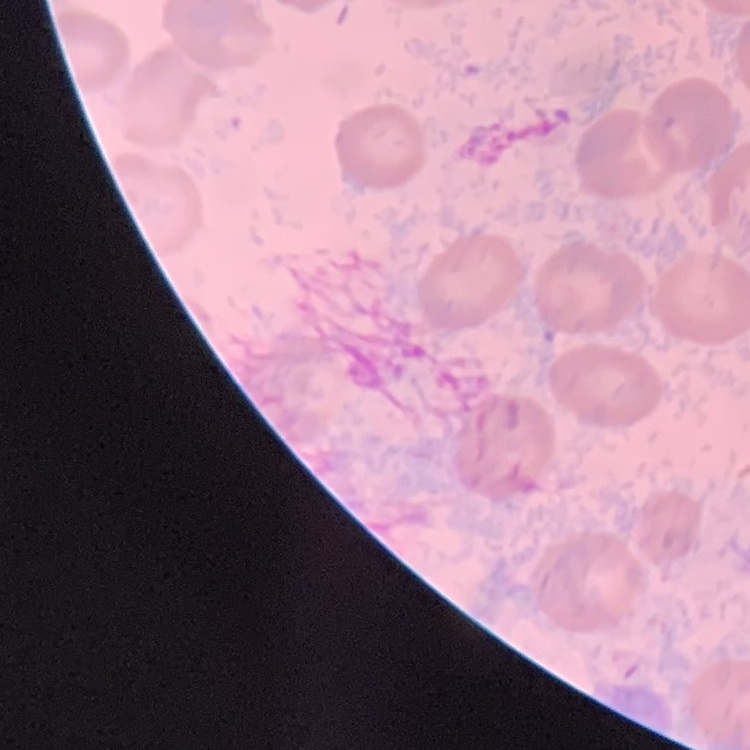

The red blood cells exhibit no rouleaux formation. One tile cut from a larger photomicrograph. Thin blood smear. Stained with either Field's or Giemsa.